State which parasite is depicted.
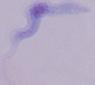
A trypanosome.

Summary:
  - Magnification: 1000x
  - Modality: photomicrograph